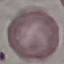

Summary:
  - Malaria status: uninfected
  - Preparation: thin smear
  - Image type: automatically extracted cell patch, resized to 64 × 64 pixels
  - Stain: Giemsa
  - Capture: smartphone camera at the microscope eyepiece